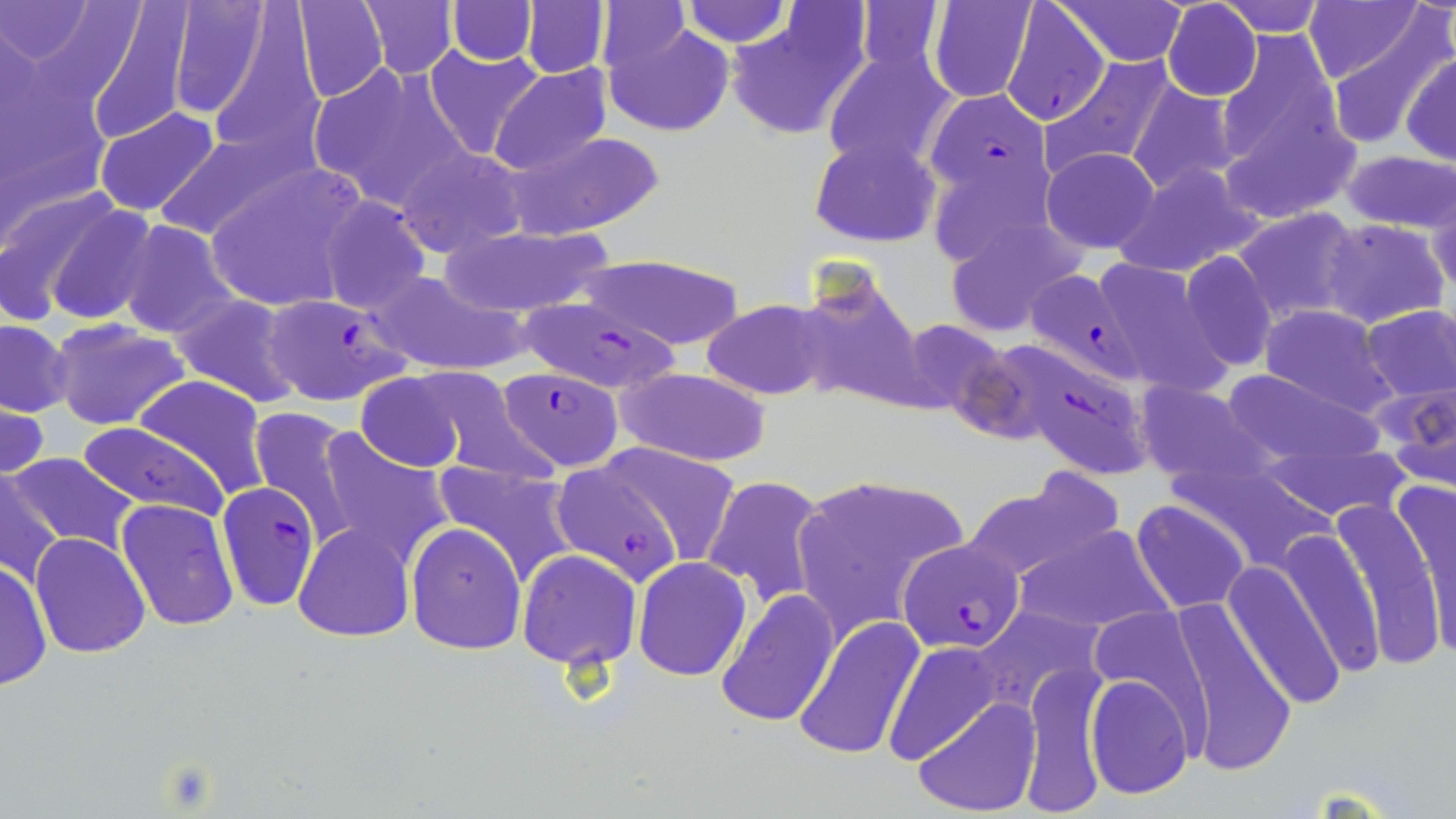
Approximate bounding boxes as [x1, y1, x2, y2] in pixels. Plasmodium falciparum-infected red blood cell locations: [999, 2, 1111, 128], [924, 87, 1051, 220], [1030, 269, 1148, 379], [259, 293, 414, 407], [511, 297, 682, 395], [999, 345, 1148, 485], [496, 364, 626, 473], [551, 461, 687, 586], [220, 486, 320, 605], [898, 537, 1027, 653]. Uninfected red blood cell locations: [0, 0, 94, 64], [166, 0, 276, 122], [289, 0, 389, 103], [358, 0, 459, 79], [446, 0, 539, 64], [522, 0, 609, 79], [679, 0, 793, 48], [1305, 0, 1422, 84], [84, 1, 196, 144], [1058, 1, 1186, 65], [1161, 1, 1262, 102], [1218, 1, 1329, 36], [595, 2, 689, 75], [926, 3, 1041, 105], [724, 8, 868, 141], [1318, 9, 1452, 146], [603, 16, 734, 138], [1222, 30, 1353, 182], [423, 46, 546, 162], [822, 47, 958, 175], [1402, 52, 1456, 166], [1038, 54, 1180, 180], [0, 57, 110, 232], [307, 61, 468, 209], [490, 64, 613, 177], [1126, 81, 1240, 196], [94, 108, 220, 218], [148, 128, 309, 243], [503, 130, 666, 239], [810, 134, 942, 248], [396, 146, 527, 257], [1039, 146, 1162, 254], [1342, 150, 1456, 234], [1111, 161, 1266, 278], [204, 163, 366, 315], [1428, 182, 1456, 299], [18, 193, 157, 328], [317, 194, 433, 314], [1233, 207, 1365, 325], [942, 216, 1088, 339], [1323, 218, 1448, 330], [115, 220, 241, 341], [437, 225, 617, 317], [1177, 251, 1278, 372], [581, 253, 744, 349], [1088, 256, 1235, 395], [369, 270, 526, 376], [793, 273, 927, 414], [169, 293, 307, 408], [701, 298, 836, 401], [1360, 303, 1455, 405], [1258, 304, 1399, 417], [895, 318, 1014, 418], [1, 319, 74, 417], [50, 320, 191, 432], [407, 367, 551, 483], [614, 367, 773, 467], [1218, 368, 1381, 464], [356, 370, 471, 474], [132, 374, 272, 500], [1373, 378, 1455, 490], [1136, 381, 1271, 487], [0, 395, 50, 484], [248, 407, 362, 549], [77, 421, 229, 524], [310, 429, 454, 569], [1256, 434, 1416, 523], [598, 444, 741, 567], [7, 450, 141, 557], [431, 459, 582, 584], [1, 470, 64, 590], [790, 471, 968, 634], [701, 474, 830, 609], [964, 475, 1121, 582], [1389, 477, 1456, 660], [1331, 493, 1446, 669], [117, 499, 239, 631], [1131, 499, 1250, 613], [406, 521, 528, 654], [293, 523, 415, 641], [1014, 524, 1171, 636], [1279, 526, 1382, 677], [30, 532, 152, 658], [516, 550, 641, 671], [633, 556, 752, 681], [0, 557, 51, 693], [1223, 561, 1344, 711], [714, 587, 838, 727], [973, 603, 1107, 715], [1173, 605, 1297, 777], [797, 617, 926, 762], [885, 639, 1002, 765], [1020, 665, 1109, 816], [1085, 672, 1194, 801], [913, 696, 1038, 815]. Slide-level diagnosis: Plasmodium falciparum. Thin blood smear. 1000x magnification. One field of a larger specimen. May-Grünwald-Giemsa-stained preparation. Image is 1456×819 pixels. Optical microscopy.